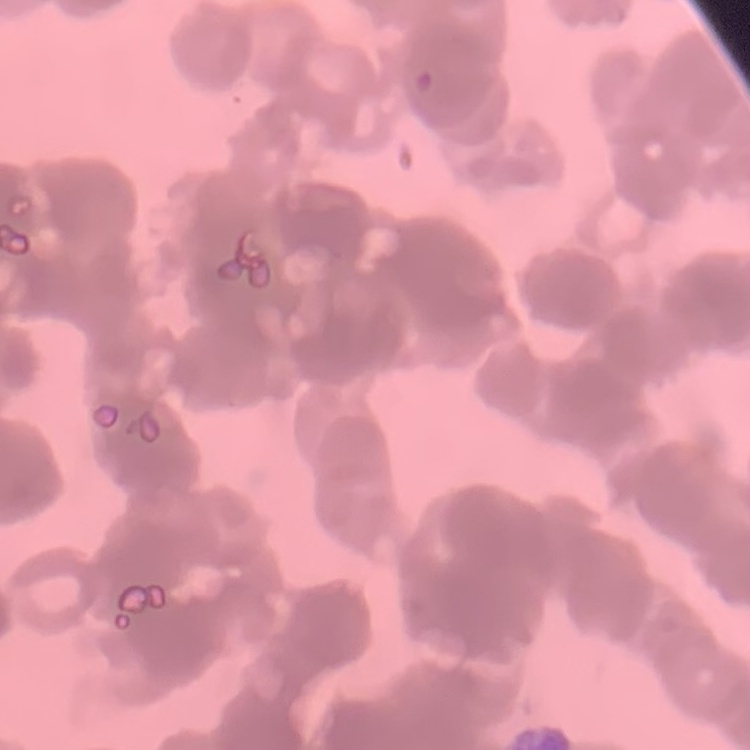
Summary:
  - Red blood cell morphology: rouleaux formation
  - Image type: one tile cut from a larger photomicrograph
  - Preparation: thin blood film
  - Stain: Field's or Giemsa